Report the malaria status of this cell.
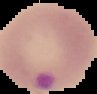
Parasitized.

Summary:
  - Image size: 97×94 pixels
  - Image type: cell region segmented out of the field of view; surrounding area masked to black
  - Preparation: thin blood film